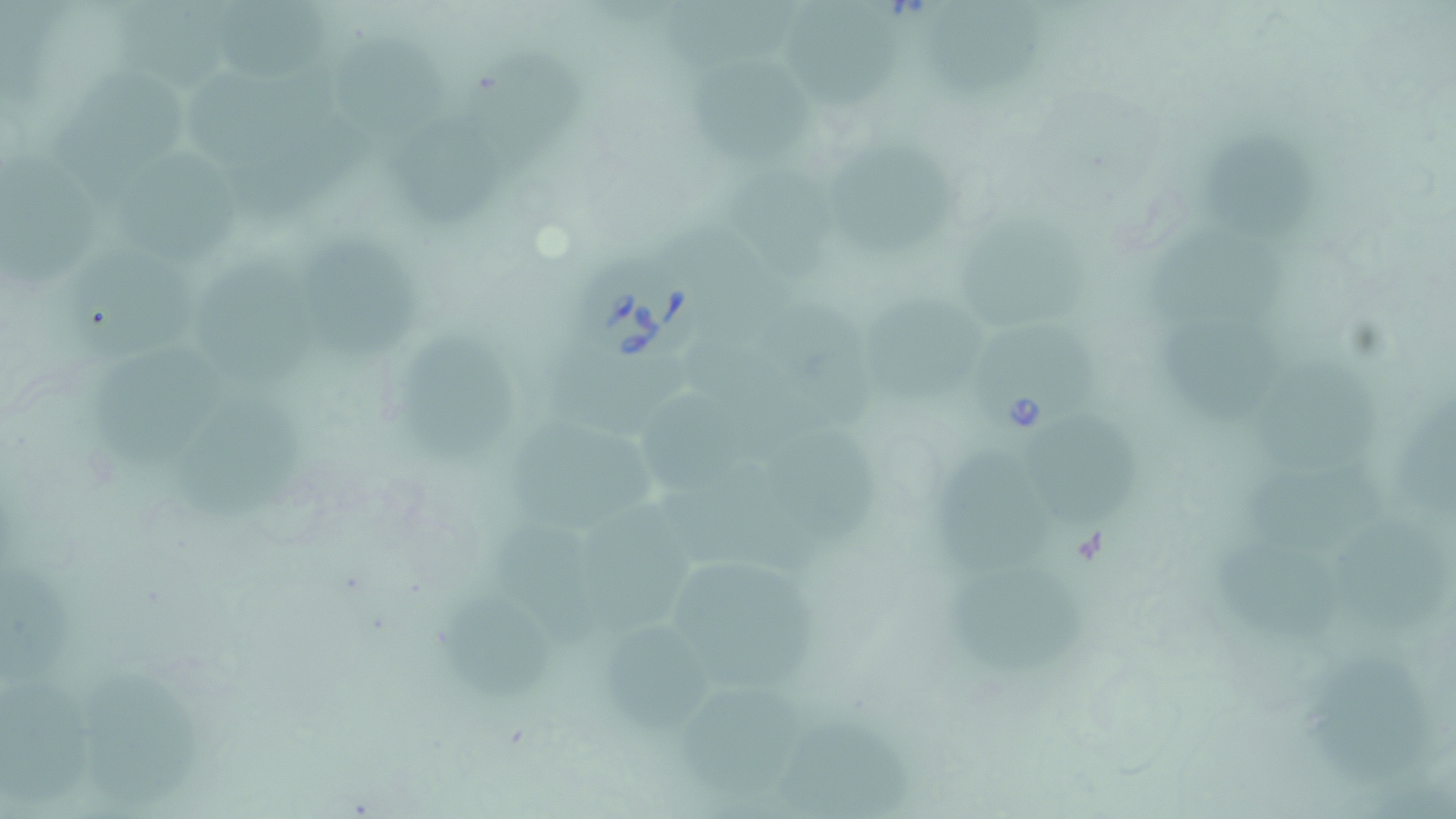
slide-level diagnosis = Babesia divergens
preparation = thin blood film
Babesia divergens-infected red blood cell locations = approximate bounding boxes as [x1, y1, x2, y2] in pixels: [575, 257, 716, 365], [980, 333, 1098, 435]
image size = 1456×819 pixels
stain = May-Grünwald-Giemsa
field of view = one of a larger specimen
uninfected red blood cell locations = approximate bounding boxes as [x1, y1, x2, y2] in pixels: [662, 2, 798, 78], [123, 3, 243, 105], [221, 3, 338, 84], [791, 10, 905, 112], [941, 13, 1060, 93], [343, 30, 448, 137], [472, 47, 597, 155], [196, 66, 340, 156], [701, 68, 819, 166], [59, 69, 192, 204], [231, 113, 373, 222], [408, 129, 511, 227], [851, 135, 968, 243], [1201, 136, 1327, 238], [0, 143, 103, 286], [117, 144, 247, 263], [725, 168, 841, 273], [971, 207, 1095, 325], [673, 211, 791, 314], [1144, 223, 1304, 321], [310, 234, 425, 376], [76, 241, 198, 359], [206, 243, 334, 393], [776, 293, 877, 422], [867, 296, 989, 408], [1157, 310, 1280, 415], [409, 336, 523, 451], [678, 345, 831, 455], [84, 348, 224, 470], [551, 357, 689, 432], [1266, 364, 1375, 464], [153, 391, 295, 529], [1393, 393, 1456, 529], [645, 400, 757, 494], [1034, 417, 1140, 526], [508, 434, 661, 532], [936, 444, 1078, 584], [796, 450, 887, 541], [1239, 454, 1386, 540], [674, 474, 835, 586], [590, 498, 706, 633], [501, 515, 605, 652], [1339, 526, 1451, 643], [1211, 534, 1342, 631], [1, 554, 92, 683], [685, 554, 831, 694], [941, 570, 1101, 679], [448, 596, 554, 700], [601, 613, 694, 737], [1307, 658, 1428, 785], [1, 664, 111, 810], [666, 672, 820, 809], [80, 682, 206, 805], [778, 710, 912, 817]
modality = optical microscopy
magnification = 1000x